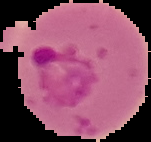

image_size: 151×142 pixels
image_type: segmented cell region on a black background
result: Plasmodium parasites identified
preparation: thin blood film